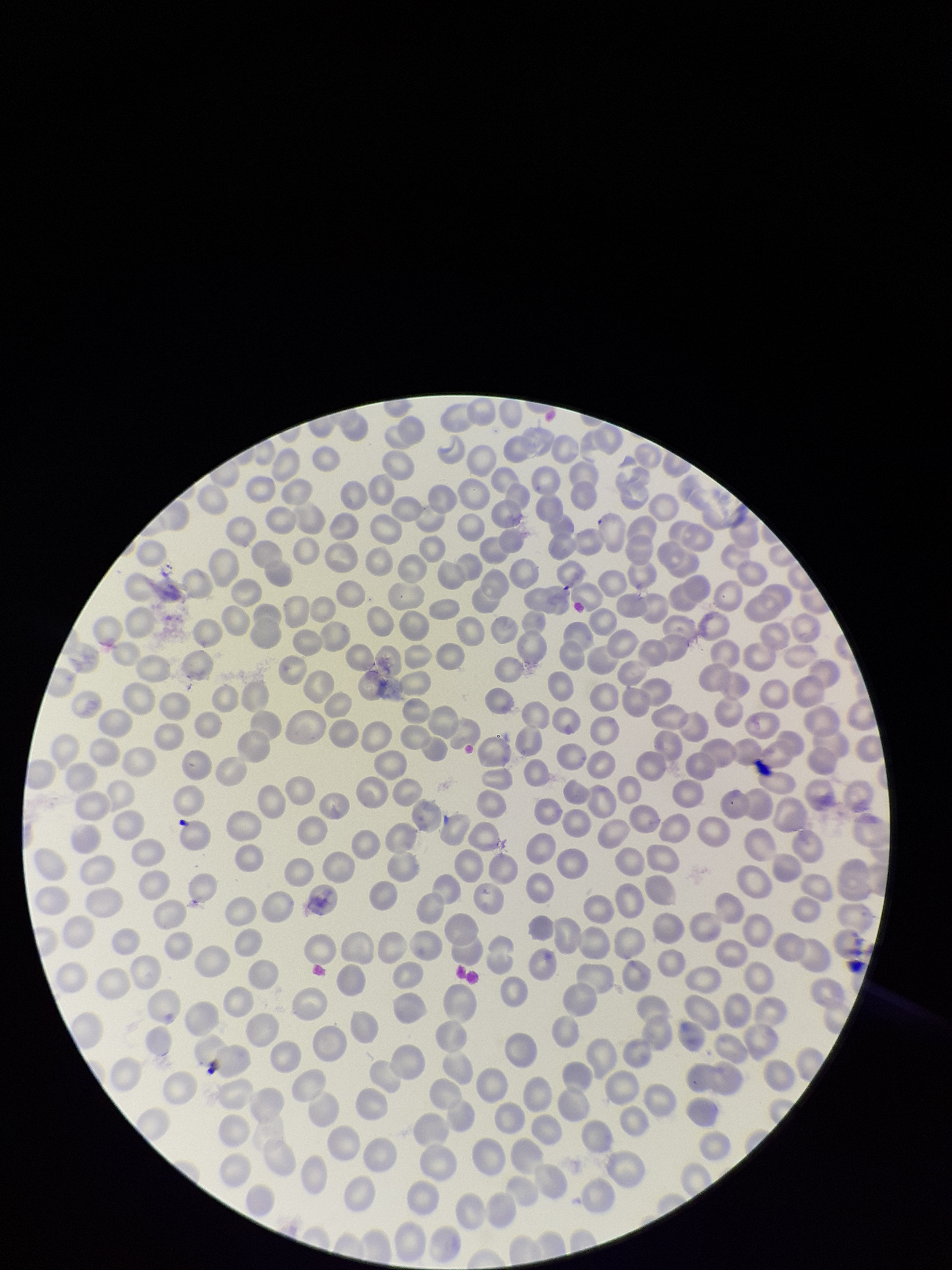
Species reported for this patient: Plasmodium falciparum. Preparation: thin blood smear. Single field of view. Patient malaria status: positive. Stained with Giemsa. Photographed through the microscope eyepiece with a smartphone camera. Image is 952×1270 pixels. Parasitized red blood cell count: 0. Parasitized red blood cells: none seen. Red blood cell count: 320.